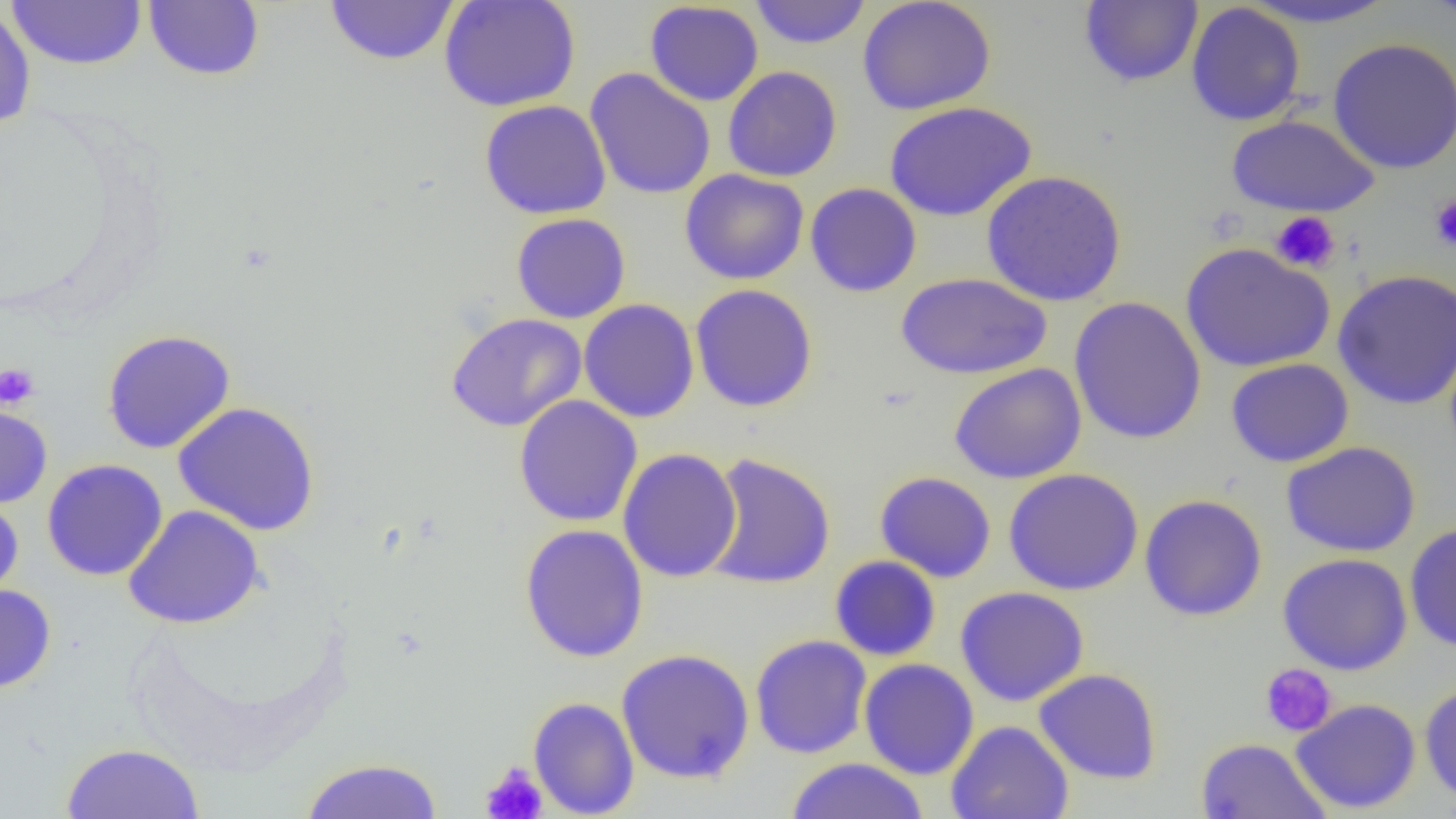

Summary:
  - Coordinate format: approximate bounding boxes as (x1,y1)-(x2,y2) corner pairs in pixels
  - Uninfected red blood cell locations: (6,0)-(147,70), (324,0)-(460,66), (439,0)-(581,112), (748,0)-(872,49), (856,0)-(996,116), (1238,0)-(1400,29), (1421,0)-(1456,25), (143,1)-(265,81), (1079,1)-(1203,88), (644,2)-(764,106), (1186,2)-(1306,126), (0,5)-(36,129), (1327,37)-(1456,174), (722,66)-(842,182), (585,68)-(716,200), (479,100)-(611,220), (884,101)-(1036,222), (1226,114)-(1380,217), (680,169)-(809,285), (981,169)-(1127,306), (805,182)-(922,298), (511,212)-(631,324), (1180,243)-(1335,372), (1332,268)-(1456,410), (896,272)-(1052,380), (690,283)-(818,412), (1068,296)-(1207,445), (579,299)-(700,423), (445,312)-(587,432), (102,329)-(235,454), (1225,358)-(1355,468), (949,363)-(1086,483), (513,395)-(643,527), (0,399)-(53,508), (173,401)-(320,537), (1282,441)-(1421,558), (618,448)-(743,582), (702,452)-(836,590), (41,459)-(169,581), (1003,467)-(1144,595), (875,471)-(997,583), (0,493)-(24,604), (1139,493)-(1268,621), (122,505)-(265,629), (1404,522)-(1456,653), (519,524)-(649,663), (1277,552)-(1413,675), (829,555)-(941,661), (0,584)-(57,693), (955,586)-(1089,707), (750,634)-(873,759), (615,648)-(755,784), (859,658)-(979,780), (1033,667)-(1162,785), (1419,680)-(1456,805), (528,696)-(640,818), (1290,698)-(1422,814), (946,720)-(1074,819), (1195,737)-(1331,818), (61,742)-(204,819), (298,757)-(445,818), (785,758)-(929,818)
  - Platelet locations: (1429,195)-(1456,251), (1270,211)-(1340,273), (0,363)-(39,409), (1259,663)-(1338,737), (480,761)-(548,819)
  - Slide-level diagnosis: no evidence of blood parasites
  - Image size: 1456×819 pixels
  - Preparation: thin blood film
  - Field of view: single
  - Magnification: 1000x
  - Modality: light microscopy